Classify this cell by malaria status.
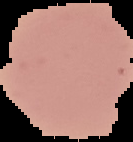
It is uninfected.

preparation = thin blood film
image type = cell region segmented out of the field of view; surrounding area masked to black
image size = 133×142 pixels